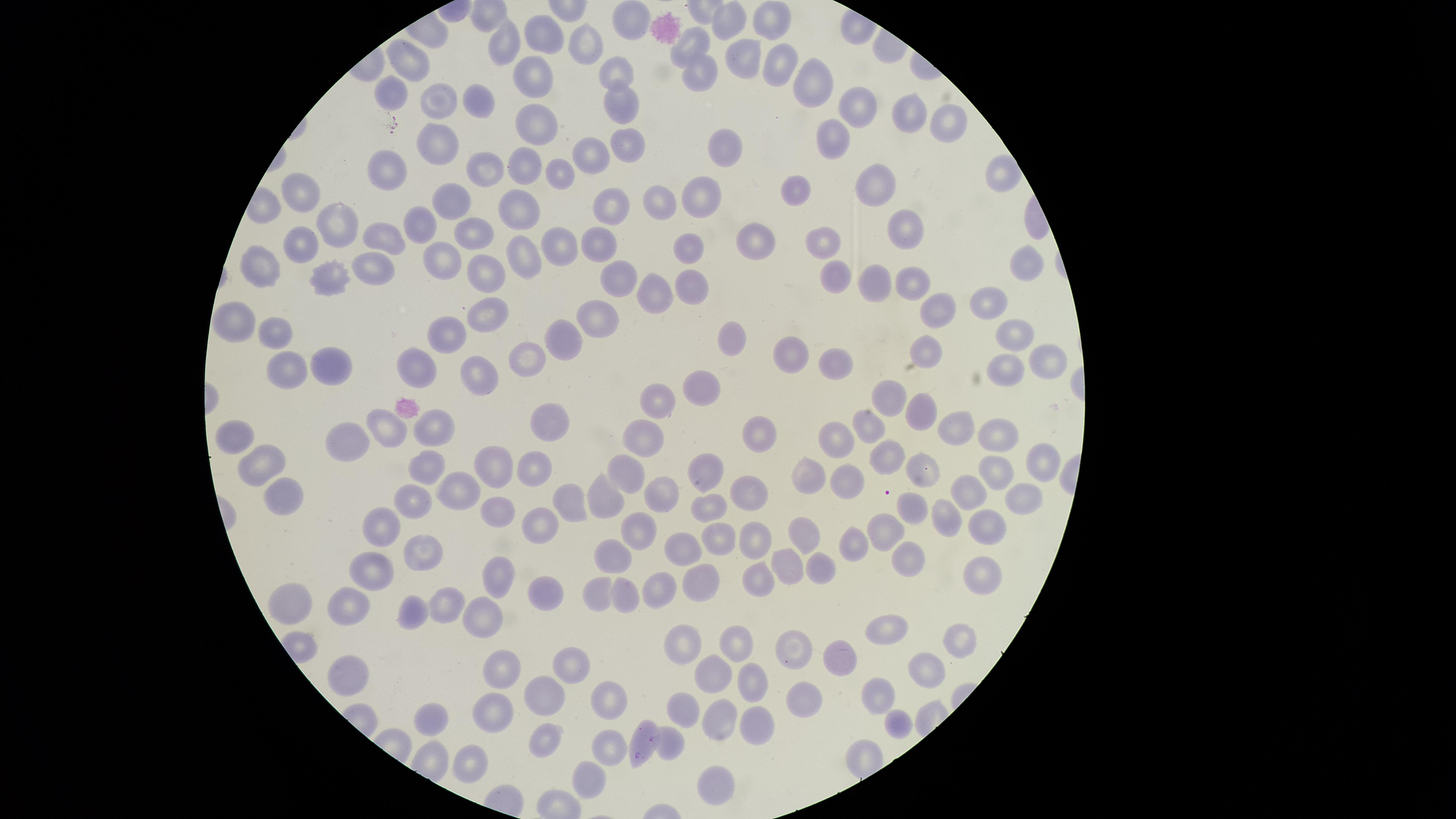
Approximate marker points, in pixels from the top-left corner. Uninfected red blood cells: (x=632, y=19), (x=770, y=23), (x=727, y=25), (x=540, y=35), (x=506, y=41), (x=591, y=43), (x=691, y=46), (x=748, y=56), (x=777, y=69), (x=610, y=75), (x=696, y=77), (x=535, y=79), (x=815, y=81), (x=478, y=96), (x=620, y=98), (x=856, y=110), (x=903, y=118), (x=944, y=125), (x=539, y=127), (x=832, y=139), (x=627, y=142), (x=726, y=149), (x=593, y=156), (x=527, y=161), (x=486, y=164), (x=382, y=169), (x=557, y=172), (x=870, y=189), (x=306, y=193), (x=799, y=194), (x=704, y=198), (x=453, y=199), (x=661, y=203), (x=522, y=206), (x=608, y=210), (x=419, y=223), (x=339, y=225), (x=475, y=232), (x=907, y=233), (x=387, y=235), (x=753, y=238), (x=600, y=244), (x=558, y=246), (x=829, y=246), (x=299, y=248), (x=693, y=248), (x=526, y=252), (x=439, y=253), (x=271, y=267), (x=1017, y=268), (x=369, y=269), (x=483, y=270), (x=835, y=273), (x=334, y=278), (x=619, y=278), (x=910, y=282), (x=872, y=285), (x=690, y=288), (x=648, y=294), (x=987, y=302), (x=486, y=305), (x=940, y=310), (x=598, y=314), (x=236, y=323), (x=277, y=334), (x=564, y=335), (x=1010, y=335), (x=448, y=336), (x=732, y=339), (x=931, y=352), (x=791, y=355), (x=1039, y=356), (x=531, y=364), (x=843, y=367), (x=416, y=368), (x=285, y=370), (x=1007, y=373), (x=337, y=377), (x=486, y=377), (x=703, y=390), (x=663, y=398), (x=896, y=398), (x=919, y=414), (x=550, y=420), (x=865, y=428), (x=956, y=429), (x=434, y=430), (x=386, y=431), (x=760, y=435), (x=643, y=436), (x=353, y=437), (x=998, y=439), (x=235, y=442), (x=835, y=445), (x=888, y=457), (x=428, y=463), (x=271, y=464), (x=1043, y=464), (x=499, y=467), (x=994, y=467), (x=626, y=470), (x=531, y=472), (x=703, y=473), (x=922, y=473), (x=810, y=477), (x=840, y=485), (x=463, y=489), (x=753, y=492), (x=602, y=493), (x=663, y=494), (x=968, y=496), (x=1028, y=498), (x=289, y=500), (x=412, y=501), (x=570, y=502), (x=912, y=510), (x=493, y=511), (x=710, y=513), (x=947, y=521), (x=543, y=522), (x=380, y=526), (x=985, y=527), (x=887, y=530), (x=640, y=531), (x=805, y=531), (x=752, y=537), (x=714, y=540), (x=856, y=543), (x=681, y=545), (x=428, y=555), (x=608, y=561), (x=911, y=561), (x=793, y=565), (x=375, y=568), (x=818, y=569), (x=497, y=573), (x=979, y=573), (x=755, y=577), (x=700, y=582), (x=656, y=589), (x=549, y=590), (x=600, y=593), (x=623, y=595), (x=294, y=597), (x=443, y=602), (x=353, y=609), (x=411, y=609), (x=485, y=610), (x=888, y=625), (x=958, y=637), (x=739, y=643), (x=792, y=650), (x=690, y=651), (x=843, y=661), (x=336, y=668), (x=573, y=670), (x=919, y=673), (x=712, y=675), (x=504, y=678), (x=753, y=684), (x=545, y=691), (x=876, y=693), (x=610, y=697), (x=803, y=698), (x=684, y=706), (x=433, y=719), (x=486, y=721), (x=751, y=722), (x=894, y=723), (x=717, y=724), (x=645, y=729), (x=549, y=738), (x=610, y=746), (x=672, y=747), (x=470, y=761), (x=589, y=780), (x=714, y=783). Single field of view. Thin smear of blood. Circular visible region. Photographed with a smartphone camera through the microscope eyepiece. Presence: no malaria parasites identified. Giemsa-stained preparation. Image is 1456×819 pixels.